Comment on the morphology of the erythrocytes.
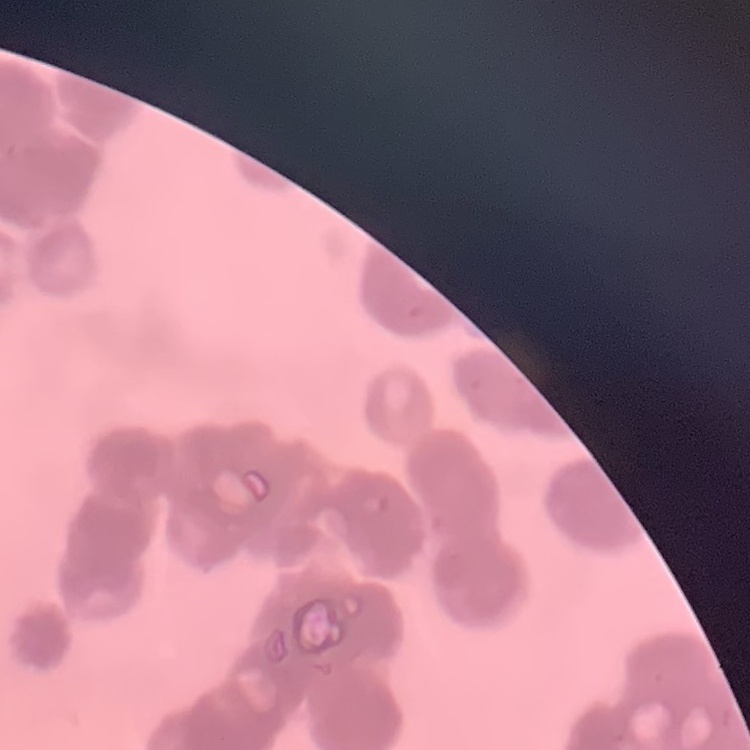
Rouleaux formation.

image_type: square crop of a larger photomicrograph
stain: Field's or Giemsa
preparation: thin blood film